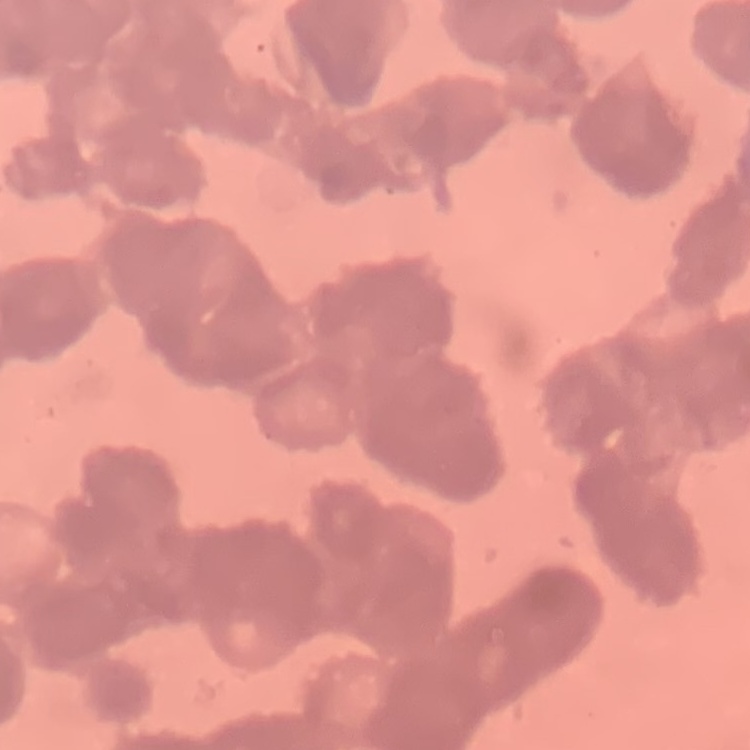

erythrocyte morphology = rouleaux formation
stain = Field's or Giemsa
preparation = thin blood smear
image type = one tile cut from a larger photomicrograph